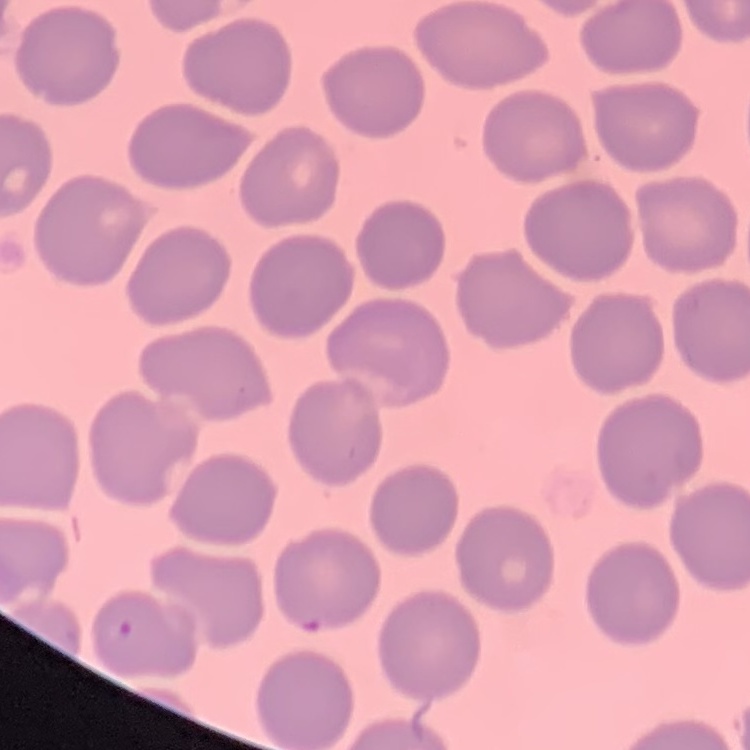
The red blood cells exhibit no rouleaux formation. Square crop of a larger photomicrograph. Thin peripheral smear. Field's or Giemsa stain.